State the preparation type.
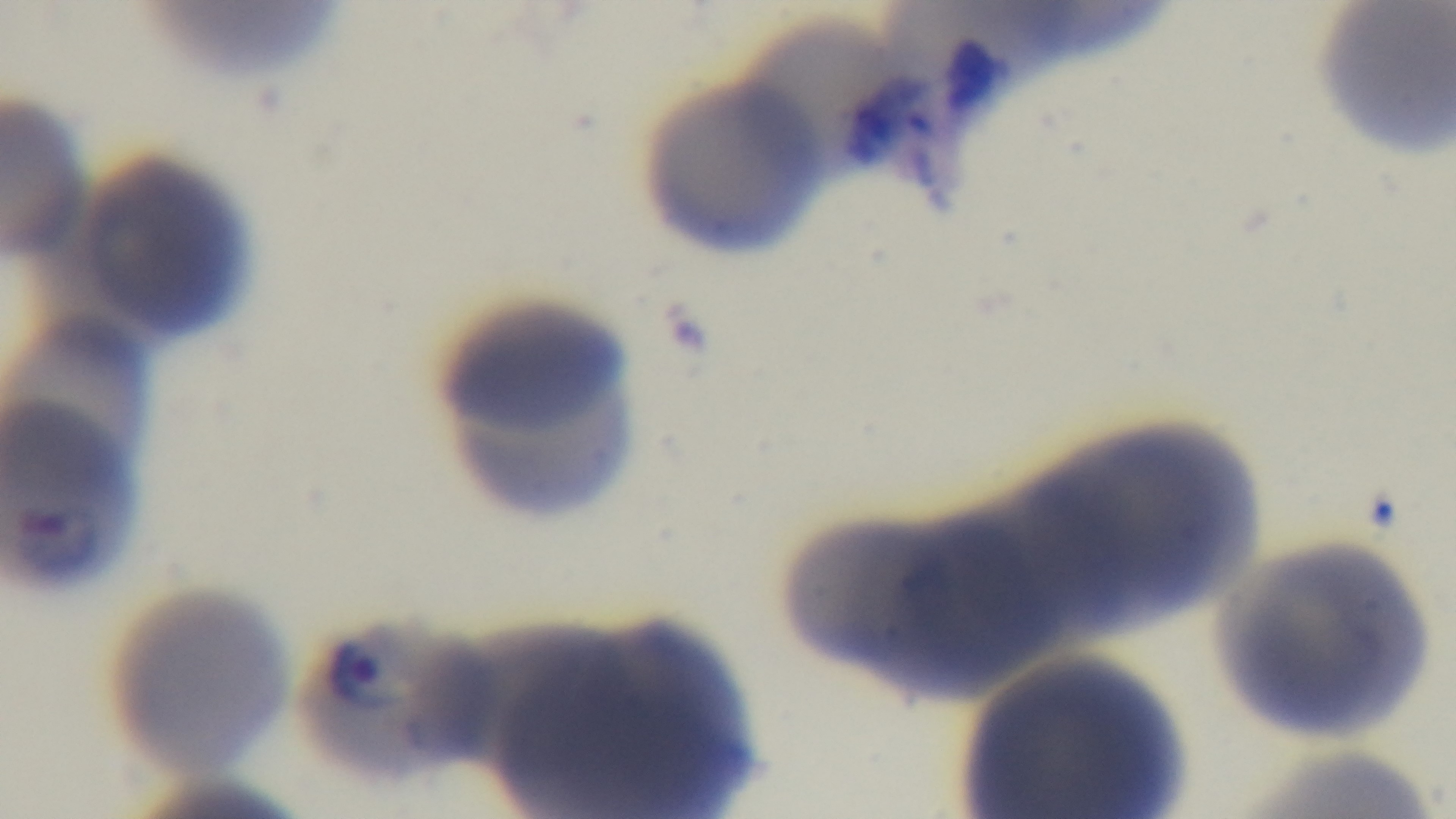

Thin.

Oil-immersion objective, 100x. Malaria status: positive. One field from the slide. Captured with a mounted 4K digital camera. Giemsa stain. Light microscopy.